Classify this cell by malaria status.
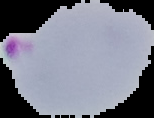

Parasitized.

Image is 154×118 pixels. Segmented cell region on a black background. From a thin blood film.